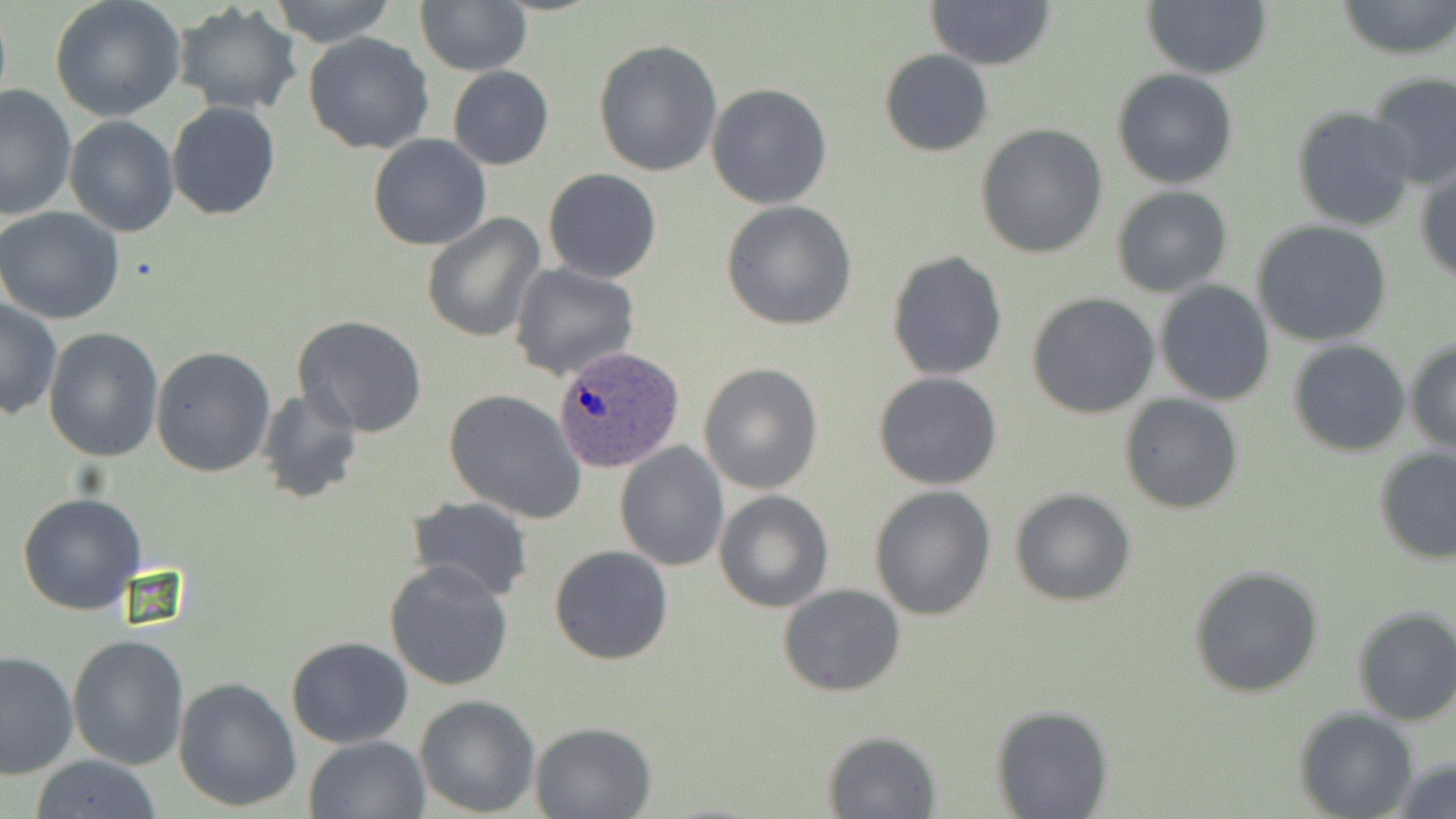

Approximate bounding boxes as (x1, y1, x2, y2) in pixels. Uninfected red blood cell locations: (49, 0, 187, 120), (268, 0, 399, 47), (926, 0, 1057, 70), (1337, 0, 1455, 60), (415, 1, 532, 75), (1141, 1, 1273, 79), (173, 3, 303, 116), (303, 33, 436, 154), (593, 39, 724, 177), (879, 49, 993, 157), (447, 66, 553, 170), (1111, 68, 1239, 189), (1366, 71, 1456, 189), (0, 83, 77, 222), (706, 83, 833, 210), (167, 102, 280, 220), (1293, 107, 1417, 230), (64, 117, 179, 237), (975, 123, 1108, 259), (368, 134, 492, 252), (1415, 164, 1456, 285), (542, 169, 661, 283), (1111, 186, 1233, 296), (721, 200, 859, 331), (0, 207, 125, 325), (421, 212, 546, 342), (1253, 221, 1393, 348), (885, 250, 1009, 381), (509, 263, 640, 383), (1154, 281, 1275, 405), (1026, 292, 1161, 418), (0, 300, 61, 420), (290, 316, 429, 439), (43, 328, 164, 463), (1405, 338, 1456, 454), (1289, 340, 1410, 456), (150, 346, 276, 477), (698, 362, 823, 495), (873, 372, 1003, 491), (254, 387, 363, 503), (444, 389, 586, 523), (1119, 393, 1246, 514), (614, 441, 729, 571), (1374, 447, 1456, 564), (869, 485, 997, 620), (714, 489, 834, 612), (1011, 489, 1135, 606), (17, 491, 146, 614), (404, 496, 533, 604), (550, 545, 674, 665), (385, 559, 515, 690), (1188, 565, 1324, 698), (778, 583, 906, 698), (1351, 606, 1456, 726), (67, 634, 189, 769), (287, 637, 414, 749), (1, 650, 76, 779), (173, 675, 303, 812), (414, 694, 540, 817), (991, 704, 1113, 819), (1295, 707, 1419, 819), (529, 721, 658, 818), (822, 731, 944, 819), (303, 734, 431, 819), (1388, 754, 1456, 819), (27, 755, 163, 819). Plasmodium ovale-infected red blood cell locations: (552, 345, 684, 474). Slide-level diagnosis: Plasmodium ovale. Thin blood film. Captured at 1000x magnification. One field of a larger specimen. Image is 1456×819 pixels. May-Grünwald-Giemsa stain. Light microscopy.